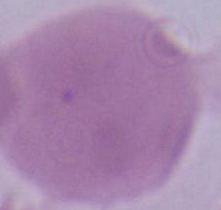
Summary:
  - Identification: erythrocyte
  - Magnification: 1000x
  - Modality: photomicrograph